Classify this cell by malaria status.
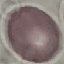

It is uninfected.

Photographed with a smartphone camera at the microscope eyepiece. Cell patch, automatically extracted from a larger field of view and resized to 64 × 64 pixels. Thin blood smear. Giemsa stain.